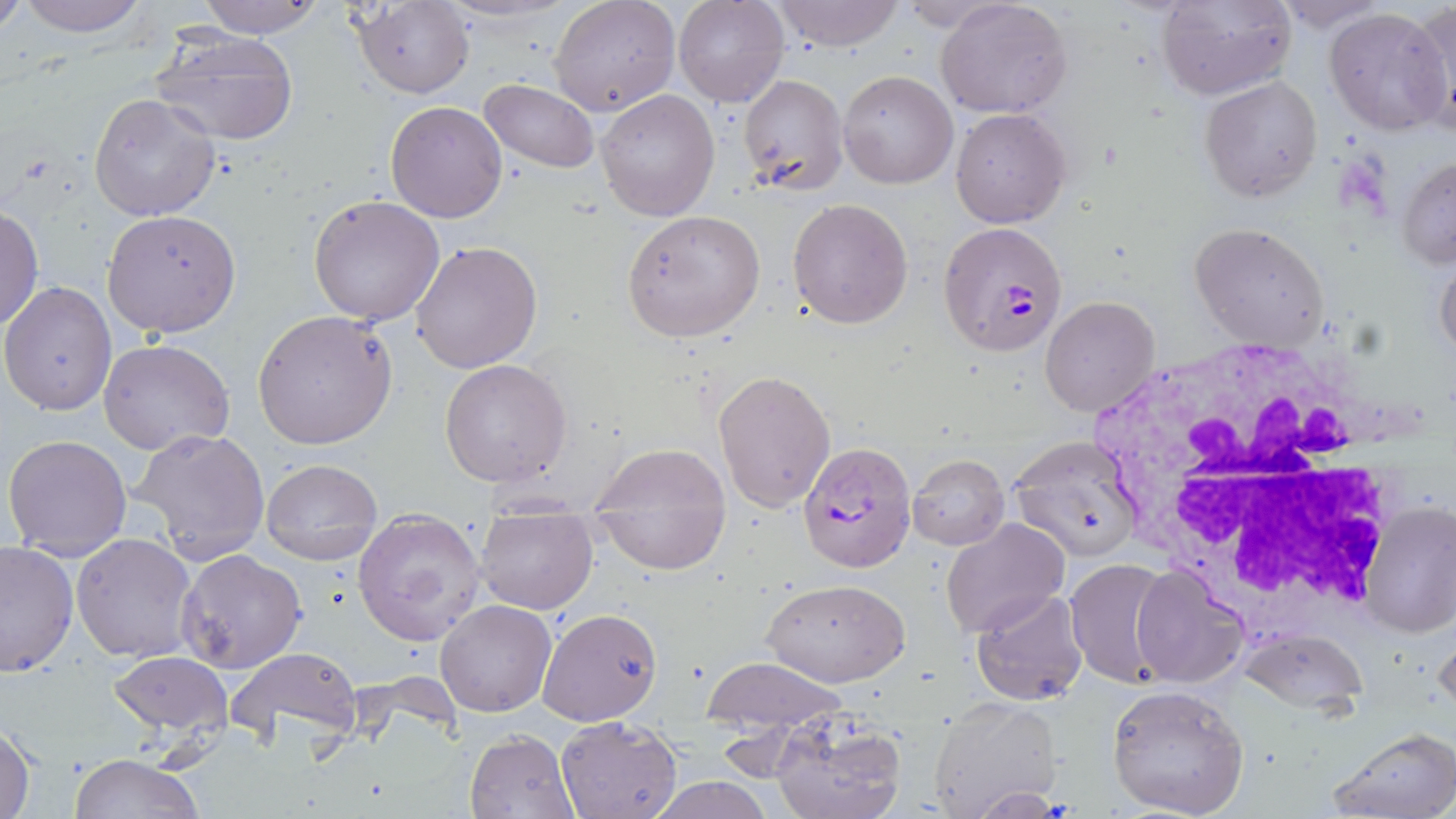

Summary:
  - Coordinate format: approximate bounding boxes as named x1/y1/x2/y2 corners in pixels
  - White blood cell locations: (x1=1081, y1=345, x2=1394, y2=618)
  - Plasmodium falciparum-infected red blood cell locations: (x1=939, y1=221, x2=1069, y2=359), (x1=796, y1=440, x2=917, y2=575)
  - Uninfected red blood cell locations: (x1=15, y1=0, x2=149, y2=38), (x1=194, y1=0, x2=329, y2=38), (x1=549, y1=0, x2=679, y2=117), (x1=674, y1=0, x2=788, y2=108), (x1=770, y1=0, x2=904, y2=50), (x1=936, y1=0, x2=1071, y2=118), (x1=1156, y1=0, x2=1296, y2=100), (x1=1273, y1=0, x2=1390, y2=32), (x1=1414, y1=0, x2=1455, y2=137), (x1=0, y1=1, x2=29, y2=34), (x1=352, y1=1, x2=474, y2=97), (x1=1324, y1=6, x2=1453, y2=135), (x1=150, y1=27, x2=300, y2=146), (x1=837, y1=69, x2=958, y2=190), (x1=737, y1=72, x2=850, y2=198), (x1=1199, y1=76, x2=1324, y2=203), (x1=478, y1=78, x2=601, y2=173), (x1=597, y1=89, x2=720, y2=221), (x1=90, y1=93, x2=222, y2=223), (x1=385, y1=101, x2=508, y2=222), (x1=949, y1=108, x2=1070, y2=227), (x1=1397, y1=155, x2=1456, y2=268), (x1=309, y1=194, x2=444, y2=325), (x1=787, y1=197, x2=913, y2=329), (x1=0, y1=206, x2=44, y2=332), (x1=623, y1=209, x2=766, y2=341), (x1=102, y1=210, x2=241, y2=337), (x1=1189, y1=222, x2=1331, y2=352), (x1=411, y1=240, x2=543, y2=374), (x1=1435, y1=248, x2=1456, y2=363), (x1=2, y1=280, x2=117, y2=415), (x1=1039, y1=294, x2=1160, y2=418), (x1=253, y1=309, x2=397, y2=451), (x1=99, y1=340, x2=235, y2=457), (x1=439, y1=359, x2=571, y2=487), (x1=713, y1=369, x2=836, y2=512), (x1=129, y1=428, x2=270, y2=563), (x1=3, y1=432, x2=133, y2=559), (x1=1006, y1=437, x2=1145, y2=559), (x1=590, y1=443, x2=732, y2=518), (x1=906, y1=453, x2=1010, y2=550), (x1=262, y1=457, x2=382, y2=565), (x1=597, y1=501, x2=722, y2=572), (x1=1359, y1=501, x2=1456, y2=639), (x1=353, y1=508, x2=487, y2=645), (x1=475, y1=508, x2=597, y2=614), (x1=941, y1=520, x2=1069, y2=639), (x1=72, y1=532, x2=197, y2=663), (x1=0, y1=541, x2=78, y2=675), (x1=176, y1=550, x2=306, y2=674), (x1=1064, y1=559, x2=1178, y2=687), (x1=1131, y1=566, x2=1248, y2=687), (x1=761, y1=576, x2=911, y2=686), (x1=971, y1=590, x2=1088, y2=705), (x1=435, y1=600, x2=557, y2=717), (x1=537, y1=607, x2=663, y2=725), (x1=1433, y1=616, x2=1456, y2=719), (x1=1236, y1=626, x2=1369, y2=716), (x1=226, y1=646, x2=363, y2=748), (x1=109, y1=651, x2=232, y2=741), (x1=701, y1=657, x2=852, y2=729), (x1=1106, y1=684, x2=1250, y2=817), (x1=927, y1=698, x2=1059, y2=818), (x1=768, y1=714, x2=908, y2=819), (x1=555, y1=715, x2=683, y2=819), (x1=1, y1=722, x2=37, y2=819), (x1=1323, y1=727, x2=1456, y2=819), (x1=464, y1=729, x2=579, y2=819), (x1=69, y1=754, x2=207, y2=818), (x1=645, y1=775, x2=778, y2=818)
  - Slide-level diagnosis: Plasmodium falciparum
  - Field of view: single
  - Image size: 1456×819 pixels
  - Modality: light microscopy
  - Stain: May-Grünwald-Giemsa
  - Preparation: thin blood film
  - Magnification: 1000x